Assess the morphology of the erythrocytes.
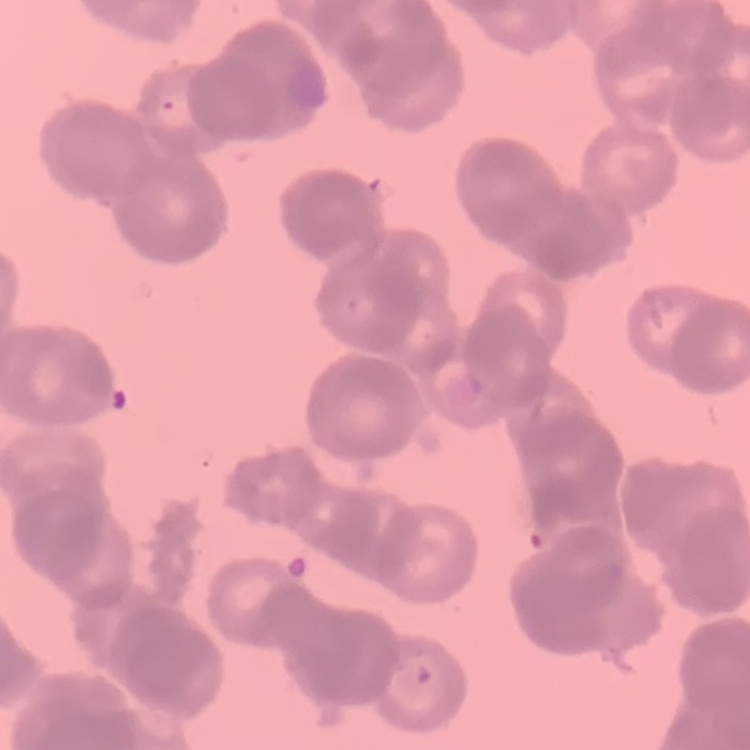

They show rouleaux formation.

One tile cut from a larger photomicrograph. Thin blood film. Stained with either Field's or Giemsa.